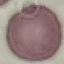 Result: negative for malaria parasites. Cell patch, automatically extracted from a larger field of view and resized to 64 × 64 pixels. Acquired by smartphone through the microscope eyepiece. Thin blood film. Giemsa-stained preparation.